State which parasite is depicted.
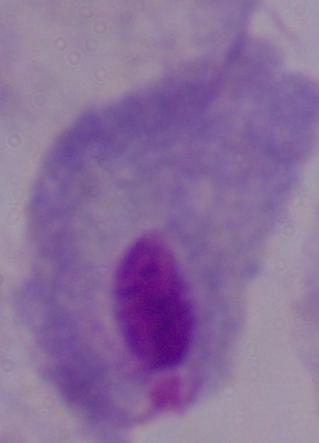

A trichomonad.

modality = micrograph
magnification = 1000x